Report the malaria status of this cell.
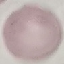

Uninfected.

Summary:
  - Capture: smartphone through the microscope eyepiece
  - Stain: Giemsa
  - Preparation: thin blood film
  - Image type: automatically extracted cell patch, resized to 64 × 64 pixels